Assess this cell for malaria.
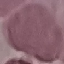

Uninfected.

Thin smear of blood. Automatically extracted cell patch, resized to 64 × 64 pixels. Giemsa stain. Photographed with a smartphone camera at the microscope eyepiece.